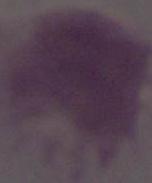
Captured at 1000x magnification. An erythrocyte is seen. Photomicrograph.